Name the parasite shown.
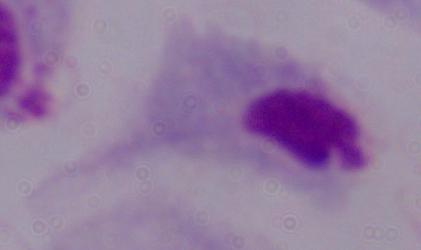

A trichomonad.

Captured at 1000x magnification. Photomicrograph.